Identify the parasite.
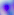
This is Toxoplasma gondii.

Captured at 400x magnification. Micrograph.